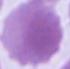
magnification = 1000x
modality = micrograph
identification = erythrocyte